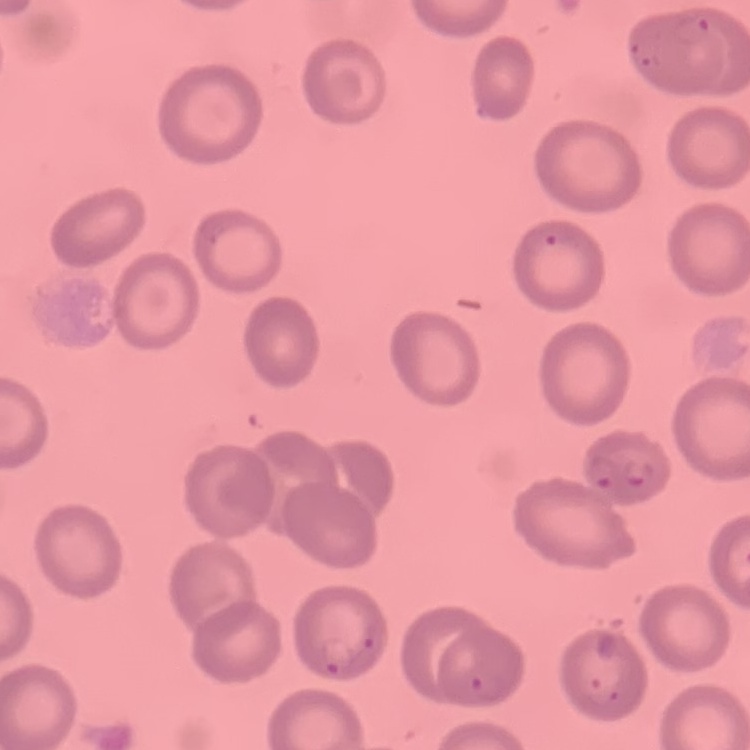

Summary:
  - Erythrocyte morphology: no rouleaux formation
  - Image type: square crop of a larger photomicrograph
  - Preparation: thin blood smear
  - Stain: Field's or Giemsa